Identify the parasite.
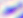
Toxoplasma gondii.

Summary:
  - Magnification: 400x
  - Modality: micrograph